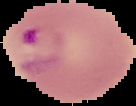 Malaria status: parasitized. Image is 136×106 pixels. From a thin blood film. Segmented cell region on a black background.